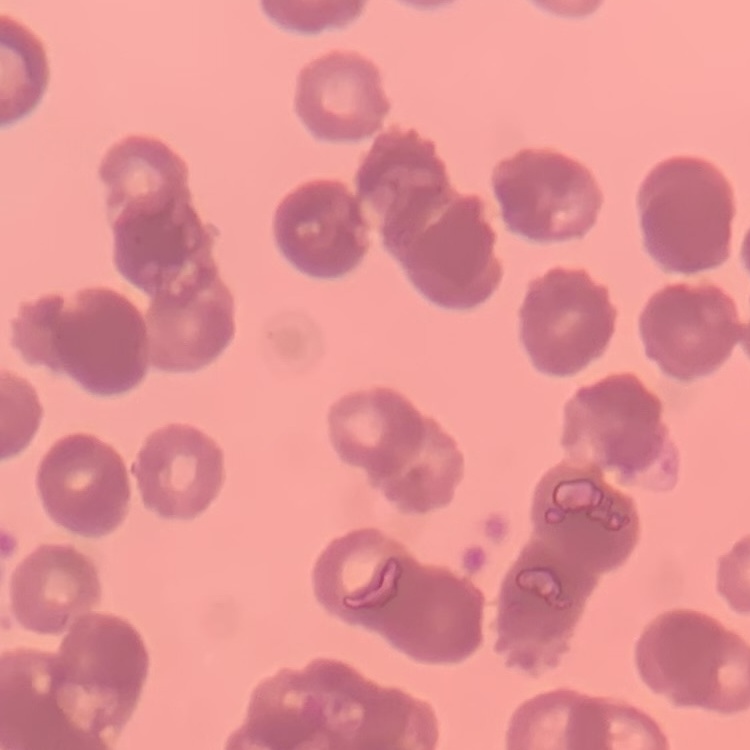 The erythrocytes show rouleaux formation. Thin blood film. One tile cut from a larger photomicrograph. Field's or Giemsa stain.